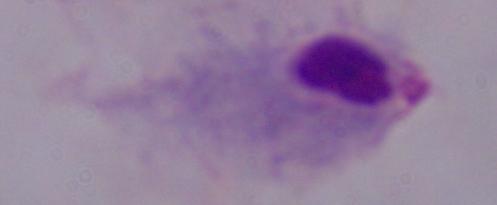

Summary:
  - Modality: micrograph
  - Magnification: 1000x
  - Identification: trichomonad